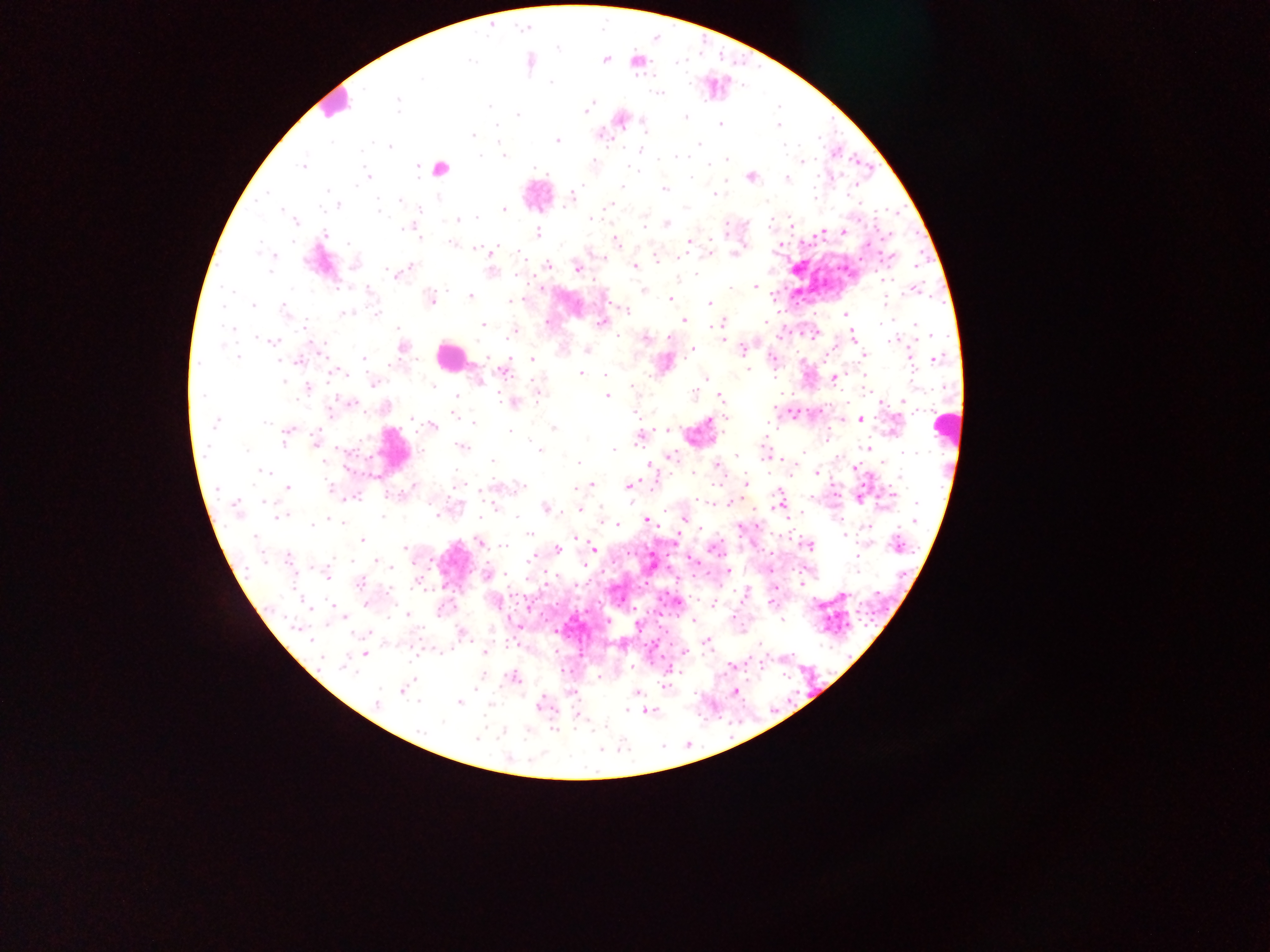
Approximate centers as (x, y) in pixels. Malaria parasite locations: (605, 59), (471, 62), (422, 79), (551, 82), (658, 94), (399, 103), (490, 105), (588, 107), (585, 111), (518, 114), (685, 117), (778, 125), (495, 126), (721, 126), (645, 127), (474, 135), (602, 135), (331, 141), (558, 141), (700, 144), (783, 145), (391, 147), (640, 150), (503, 155), (481, 156), (659, 159), (726, 159), (593, 160), (802, 161), (709, 164), (302, 166), (418, 166), (535, 167), (629, 168), (367, 176), (692, 177), (751, 177), (787, 178), (622, 187), (664, 189), (326, 191), (575, 193), (266, 194), (715, 195), (815, 196), (572, 197), (400, 200), (337, 205), (609, 205), (419, 208), (503, 209), (282, 210), (378, 210), (477, 218), (591, 219), (295, 220), (457, 220), (667, 223), (645, 225), (726, 225), (407, 227), (403, 229), (822, 232), (843, 232), (537, 233), (325, 234), (419, 237), (616, 240), (690, 241), (711, 241), (347, 242), (452, 243), (710, 246), (475, 249), (494, 249), (710, 251), (735, 254), (275, 255), (604, 258), (888, 258), (656, 260), (548, 264), (411, 266), (635, 266), (577, 269), (271, 270), (491, 271), (396, 273), (695, 274), (517, 276), (884, 279), (754, 287), (732, 288), (541, 289), (369, 290), (644, 290), (913, 291), (470, 296), (430, 299), (669, 299), (514, 300), (709, 303), (253, 306), (224, 307), (285, 310), (627, 310), (343, 314), (377, 314), (845, 314), (684, 319), (724, 322), (546, 323), (601, 323), (766, 323), (482, 324), (881, 324), (917, 326), (712, 327), (512, 333), (508, 335), (853, 337), (645, 338), (669, 338), (724, 338), (260, 339), (891, 340), (273, 342), (403, 347), (692, 350), (743, 350), (587, 351), (864, 355), (238, 356), (364, 358), (911, 358), (937, 358), (532, 359), (773, 359), (298, 361), (749, 370), (504, 371), (581, 373), (606, 374), (706, 379), (834, 379), (284, 381), (479, 381), (374, 382), (433, 386), (631, 386), (308, 388), (539, 394), (694, 394), (202, 395), (606, 396), (457, 397), (721, 397), (513, 402), (349, 403), (903, 403), (456, 415), (460, 417), (725, 418), (412, 419), (860, 420), (265, 422), (474, 422), (215, 423), (433, 426), (554, 429), (667, 429), (290, 430), (510, 431), (286, 435), (315, 438), (640, 438), (283, 443), (462, 446), (867, 448), (540, 450), (613, 450), (737, 455), (671, 456), (324, 461), (492, 461), (578, 463), (717, 464), (649, 466), (855, 468), (264, 472), (694, 473), (816, 473), (899, 479), (746, 483), (591, 485), (414, 486), (629, 486), (288, 487), (330, 487), (520, 487), (697, 499), (265, 501), (730, 502), (916, 503), (235, 505), (267, 507), (546, 508), (579, 510), (283, 515), (436, 515), (383, 516), (517, 517), (332, 520), (915, 520), (647, 521), (312, 524), (867, 526), (529, 534), (844, 536), (254, 538), (362, 541), (478, 542), (808, 545), (896, 545), (504, 546), (405, 547), (594, 548), (557, 549), (530, 558), (289, 559), (856, 560), (377, 562), (390, 565), (327, 573), (489, 574), (361, 582), (407, 615), (782, 619), (297, 627), (462, 634), (310, 638), (707, 643), (760, 644), (684, 651), (485, 653), (365, 654), (322, 657), (345, 665), (514, 676), (665, 685), (403, 689), (734, 691), (636, 693), (418, 701), (377, 703), (460, 703), (541, 704), (628, 711), (443, 722), (477, 738). Leukocyte locations: (334, 103), (440, 166), (450, 356), (947, 422). Image is 1270×952 pixels. Thick blood film. Single field of view. Photographed through a microscope with a mobile-phone camera. Sample from Ghana.